Describe the morphology of the red blood cells.
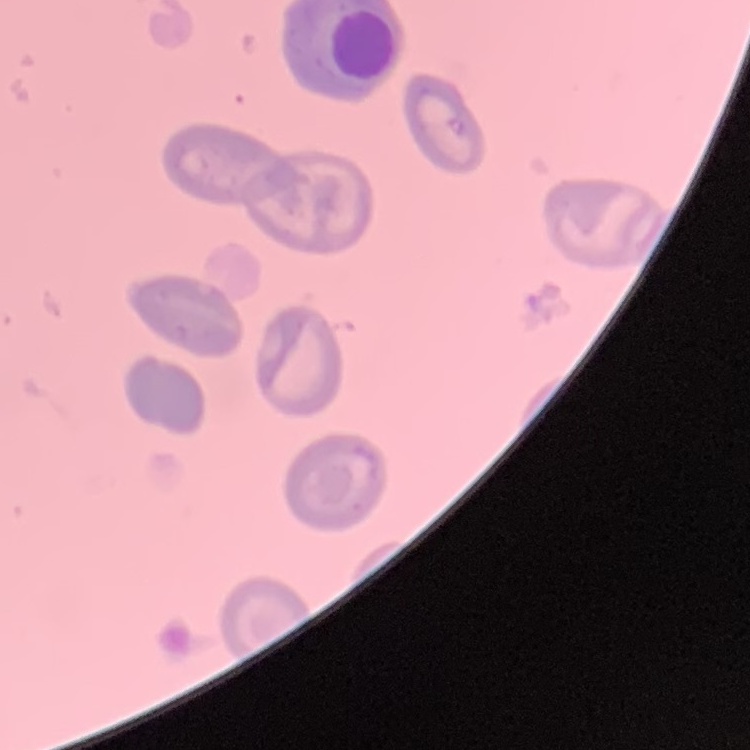
They show no rouleaux formation.

image type = one tile cut from a larger photomicrograph
stain = Field's or Giemsa
preparation = thin blood smear